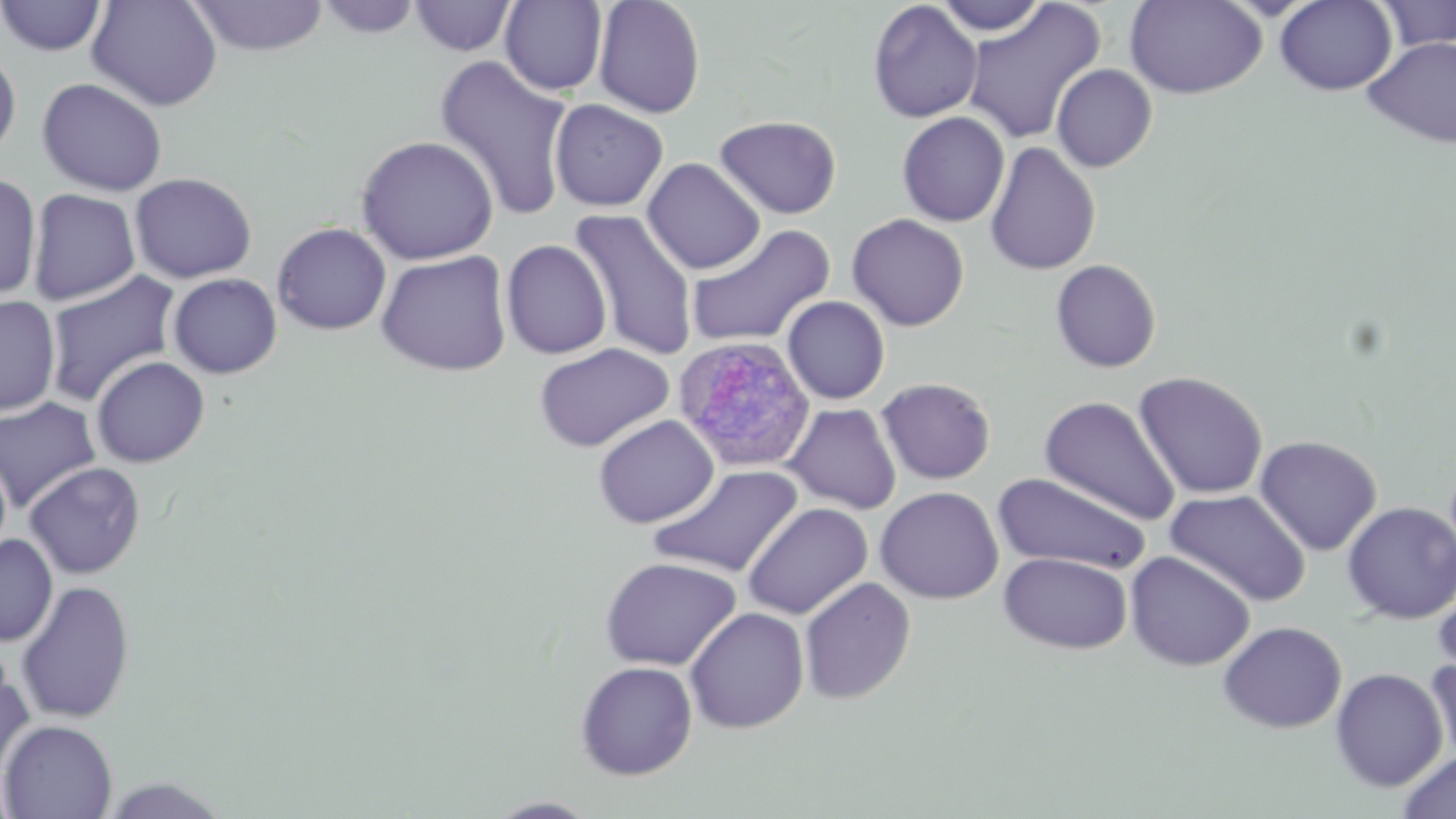
plasmodium_ovale_infected_red_blood_cell_locations: 'approximate bounding boxes as (x1,y1)-(x2,y2) corner pairs in pixels: (673,335)-(817,473)'
slide_level_diagnosis: Plasmodium ovale
preparation: thin blood film
field_of_view: one of a larger specimen
uninfected_red_blood_cell_locations: 'approximate bounding boxes as (x1,y1)-(x2,y2) corner pairs in pixels: (0,0)-(109,57), (87,0)-(223,111), (186,0)-(330,56), (316,0)-(423,40), (409,0)-(517,57), (499,0)-(608,96), (592,0)-(707,118), (932,0)-(1051,36), (1125,0)-(1267,99), (1274,0)-(1397,95), (1376,0)-(1456,52), (867,1)-(982,122), (960,2)-(1106,144), (1362,36)-(1456,148), (0,46)-(22,162), (434,54)-(575,220), (1051,64)-(1157,172), (37,77)-(168,196), (549,99)-(669,212), (896,112)-(1010,227), (714,114)-(842,219), (355,134)-(499,265), (985,141)-(1101,276), (642,157)-(766,274), (129,171)-(257,283), (0,172)-(42,301), (27,188)-(140,306), (569,208)-(701,361), (847,213)-(970,331), (271,221)-(392,335), (685,223)-(836,349), (501,239)-(612,359), (375,250)-(513,376), (1049,258)-(1162,373), (44,270)-(183,406), (167,272)-(282,379), (0,296)-(61,416), (782,296)-(890,404), (533,342)-(674,452), (90,356)-(210,468), (1133,370)-(1269,500), (876,377)-(996,485), (1039,395)-(1180,525), (0,397)-(102,513), (784,403)-(902,514), (593,415)-(719,528), (1254,435)-(1382,556), (23,461)-(146,579), (648,464)-(804,578), (993,471)-(1152,575), (875,486)-(1004,604), (1164,489)-(1312,607), (1341,501)-(1456,624), (742,502)-(873,620), (0,535)-(57,646), (1125,550)-(1256,671), (999,552)-(1133,654), (599,556)-(741,670), (799,577)-(916,705), (15,579)-(135,723), (1433,585)-(1456,682), (685,606)-(809,734), (1218,621)-(1347,734), (1425,656)-(1456,766), (574,660)-(698,780), (0,661)-(34,789), (1330,667)-(1449,793), (0,719)-(118,818), (1397,751)-(1456,819), (98,776)-(234,818), (485,796)-(601,818)'
modality: optical microscopy
magnification: 1000x
image_size: 1456×819 pixels
stain: May-Grünwald-Giemsa